Assess this cell for malaria.
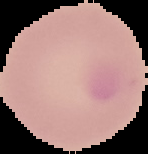
Uninfected.

Summary:
  - Image type: cell region segmented out of the field of view; surrounding area masked to black
  - Preparation: thin blood film
  - Image size: 148×154 pixels